Assess this cell for malaria.
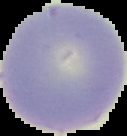

It is uninfected.

From a thin blood smear. Segmented cell region on a black background. Image is 127×136 pixels.